Describe the morphology of the red blood cells.
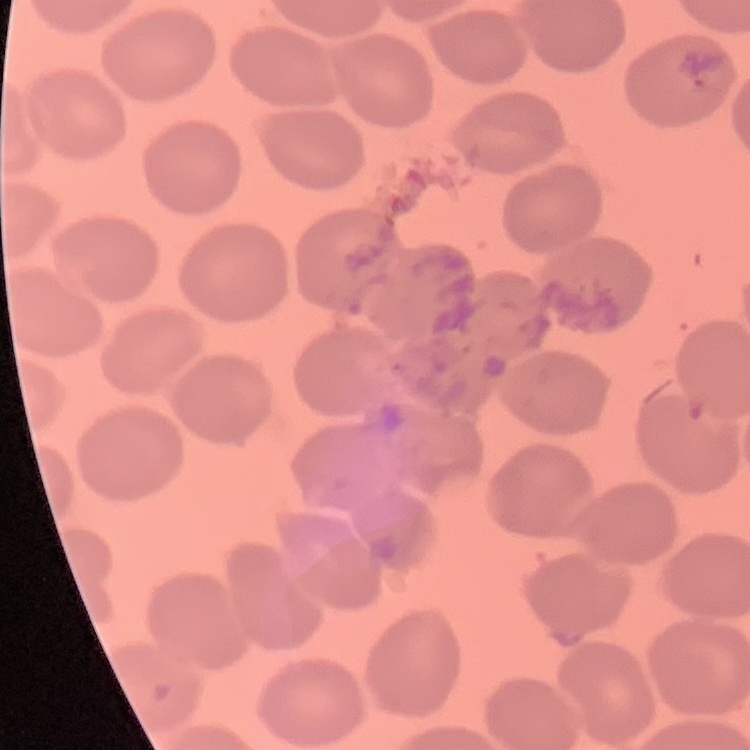
No rouleaux formation.

Summary:
  - Image type: one tile cut from a larger photomicrograph
  - Preparation: thin peripheral smear
  - Stain: Field's or Giemsa